State which cell type is depicted.
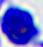
This is a leukocyte.

400x magnification. Micrograph.